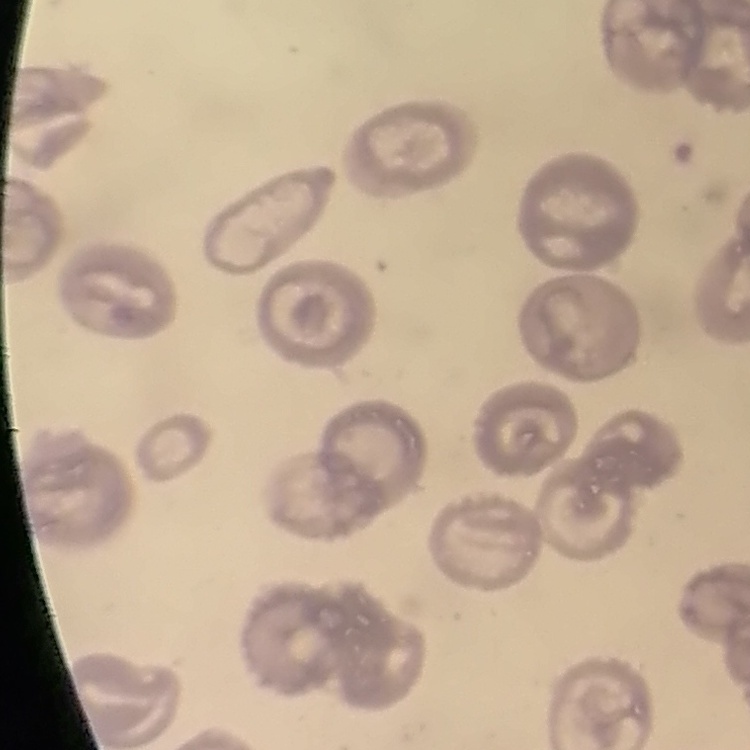
erythrocyte_morphology: no rouleaux formation
image_type: square crop of a larger photomicrograph
preparation: thin peripheral smear
stain: Field's or Giemsa